Report the malaria status of this cell.
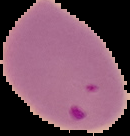

Parasitized.

preparation = thin blood smear
image type = segmented cell region on a black background
image size = 130×136 pixels